Assess this cell for malaria.
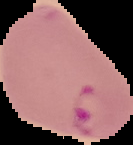

Parasitized.

From a thin blood smear. Image is 133×145 pixels. The area outside the segmented cell region is set to black.